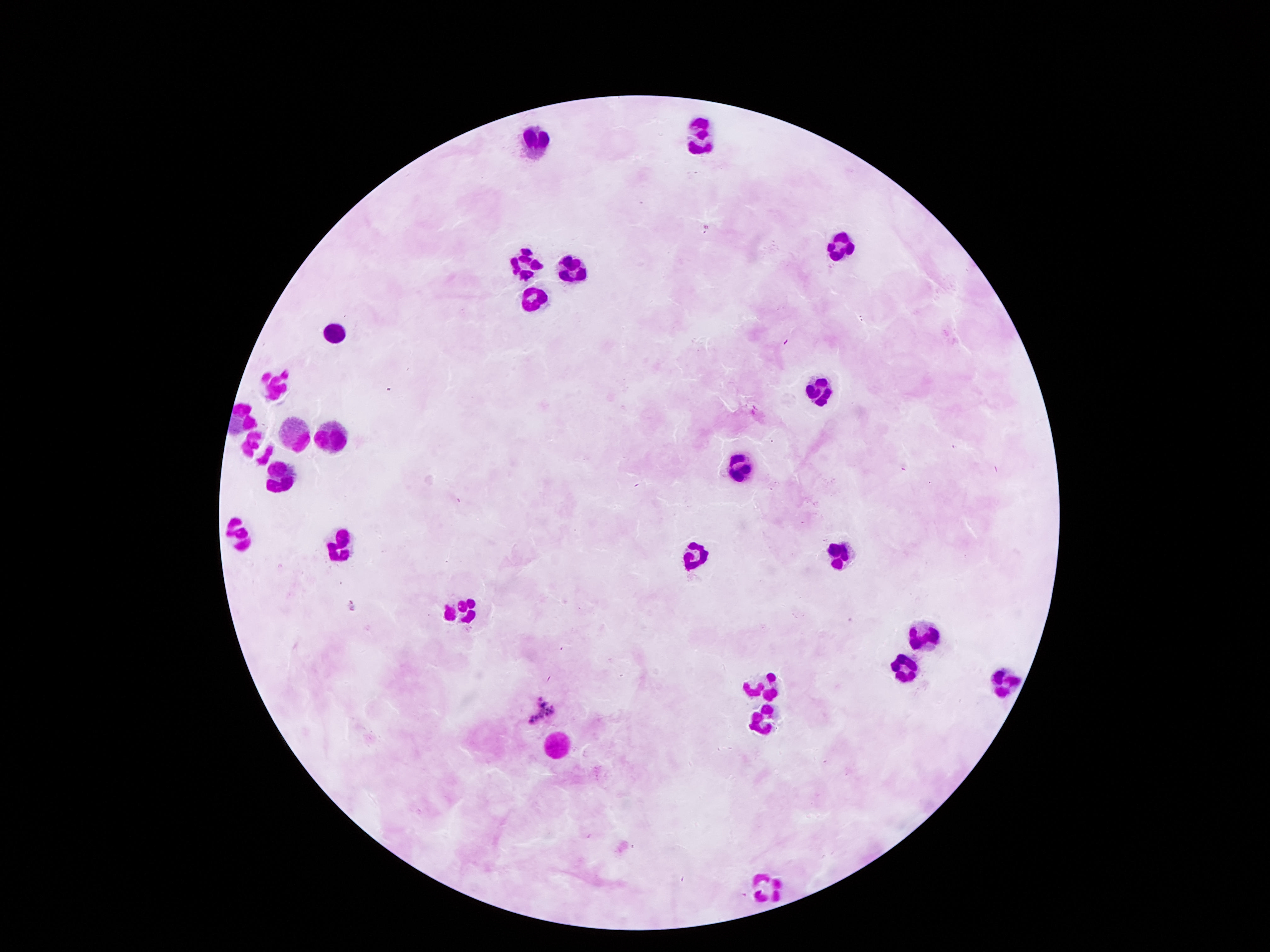

Approximate centers as (x, y) in pixels.
Summary:
  - Leukocyte locations: (698, 137), (533, 141), (834, 251), (525, 265), (573, 269), (534, 295), (331, 330), (277, 385), (815, 392), (298, 433), (333, 437), (257, 445), (739, 465), (279, 475), (240, 537), (338, 547), (694, 554), (837, 558), (462, 614), (923, 634), (904, 666), (1006, 677), (768, 686), (758, 722), (559, 749), (773, 884)
  - Capture: smartphone camera through the microscope eyepiece
  - Patient malaria status: not infected
  - Magnification: 100x
  - Image size: 1270×952 pixels
  - Field of view: one from this slide
  - Preparation: thick peripheral-blood smear
  - Stain: Giemsa